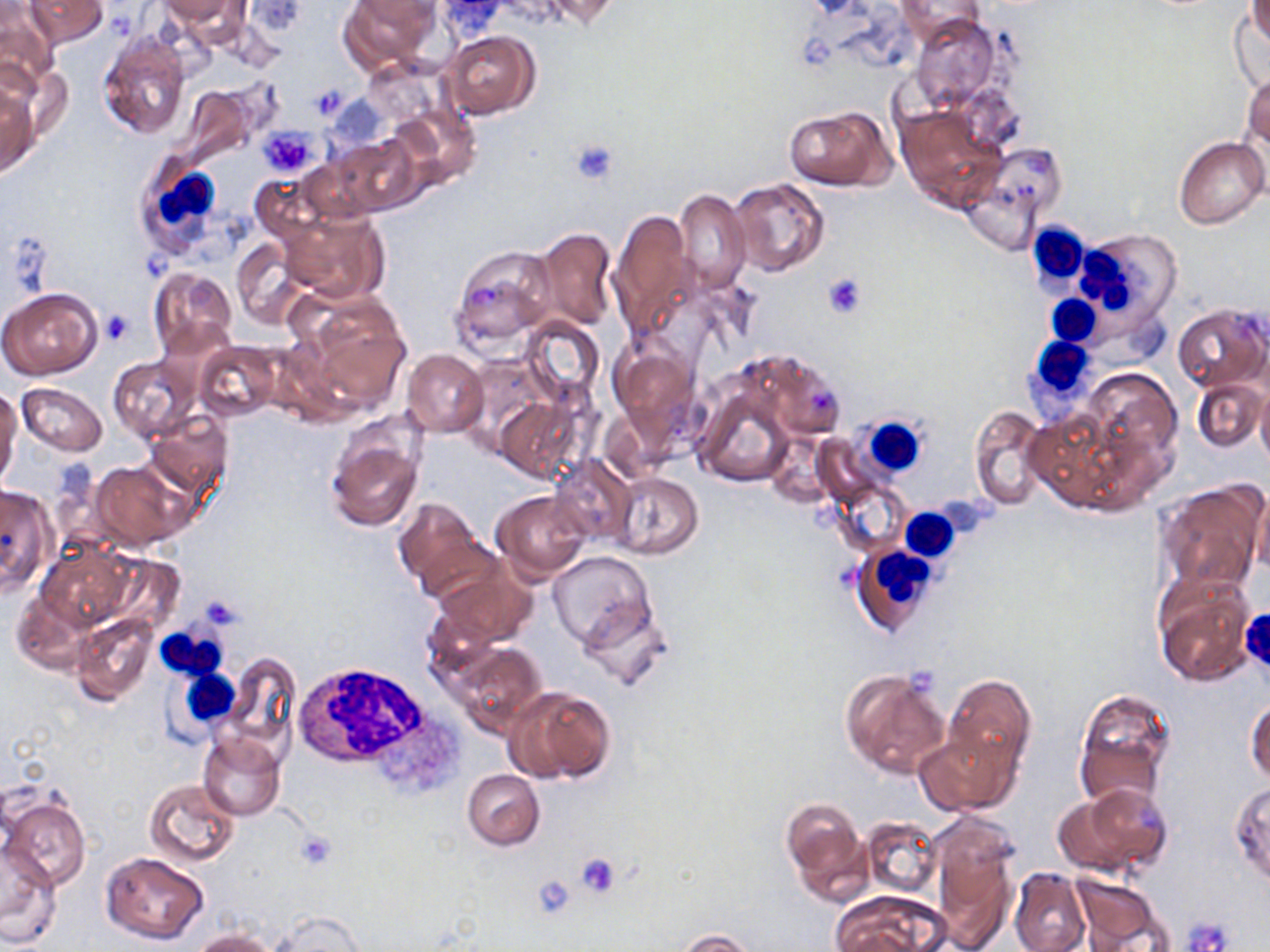
slide-level diagnosis = negative for blood parasites
stain = May-Grünwald-Giemsa
white blood cell locations = approximate bounding boxes as (x1, y1, x2, y2) in pixels: (133, 156, 225, 256), (1025, 221, 1093, 297), (1074, 230, 1182, 332), (1046, 294, 1102, 348), (1027, 337, 1096, 410), (850, 414, 935, 490), (899, 508, 960, 560), (852, 543, 939, 636), (157, 626, 227, 681), (291, 663, 445, 776), (174, 666, 242, 731)
modality = optical microscopy
uninfected red blood cell locations = approximate bounding boxes as (x1, y1, x2, y2) in pixels: (23, 0, 109, 46), (160, 0, 241, 26), (340, 0, 439, 73), (531, 0, 621, 30), (895, 0, 984, 45), (238, 1, 307, 39), (433, 1, 507, 41), (1247, 2, 1270, 47), (0, 3, 59, 90), (1231, 12, 1268, 90), (912, 15, 998, 112), (96, 29, 191, 138), (439, 30, 540, 120), (1241, 66, 1269, 160), (0, 81, 39, 178), (391, 101, 478, 185), (785, 106, 889, 190), (896, 107, 1003, 212), (329, 133, 423, 217), (1173, 136, 1268, 230), (250, 171, 332, 245), (728, 177, 830, 277), (674, 189, 750, 292), (281, 208, 389, 304), (610, 209, 694, 335), (531, 227, 617, 331), (231, 239, 310, 329), (451, 244, 557, 353), (149, 268, 236, 359), (0, 286, 103, 380), (291, 291, 412, 416), (1173, 304, 1269, 391), (521, 318, 603, 407), (608, 339, 703, 442), (195, 341, 281, 420), (742, 348, 845, 440), (401, 349, 488, 436), (460, 352, 556, 459), (108, 357, 199, 443), (1082, 367, 1182, 484), (694, 378, 798, 486), (1192, 378, 1267, 453), (16, 383, 107, 456), (1256, 386, 1270, 469), (0, 389, 20, 488), (496, 396, 581, 482), (969, 406, 1046, 508), (1026, 408, 1140, 516), (144, 410, 233, 498), (324, 421, 426, 531), (552, 457, 636, 542), (90, 460, 191, 550), (611, 472, 703, 559), (836, 481, 907, 553), (1154, 482, 1265, 596), (0, 485, 55, 595), (1249, 489, 1270, 575), (491, 490, 593, 582), (393, 497, 491, 601), (36, 541, 136, 631), (548, 551, 656, 654), (432, 563, 537, 646), (1152, 574, 1256, 687), (11, 593, 95, 673), (578, 597, 671, 693), (71, 613, 159, 707), (446, 641, 546, 734), (223, 651, 301, 752), (840, 669, 949, 779), (943, 675, 1035, 777), (507, 686, 614, 784), (1072, 689, 1177, 811), (1245, 696, 1270, 785), (915, 728, 1012, 816), (197, 734, 285, 820), (461, 770, 544, 850), (145, 778, 240, 867), (1230, 782, 1270, 889), (1060, 784, 1173, 878), (2, 792, 89, 887), (780, 797, 871, 903), (860, 817, 940, 896), (929, 820, 1015, 949), (0, 842, 62, 948), (100, 851, 210, 945), (1008, 868, 1090, 952), (526, 872, 579, 923), (1070, 876, 1166, 949), (830, 892, 947, 952), (271, 910, 365, 951), (678, 929, 757, 952), (191, 930, 275, 952)
magnification = 1000x
preparation = thin blood film
platelet locations = approximate bounding boxes as (x1, y1, x2, y2) in pixels: (312, 88, 346, 116), (261, 127, 318, 177), (569, 138, 620, 184), (821, 272, 867, 320), (100, 311, 133, 344), (196, 594, 245, 631), (293, 830, 336, 868), (577, 854, 621, 898), (532, 875, 577, 918), (1182, 917, 1233, 951)
image size = 1270×952 pixels
field of view = single